State which parasite is depicted.
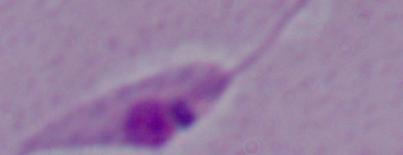

Leishmania.

Summary:
  - Modality: micrograph
  - Magnification: 1000x